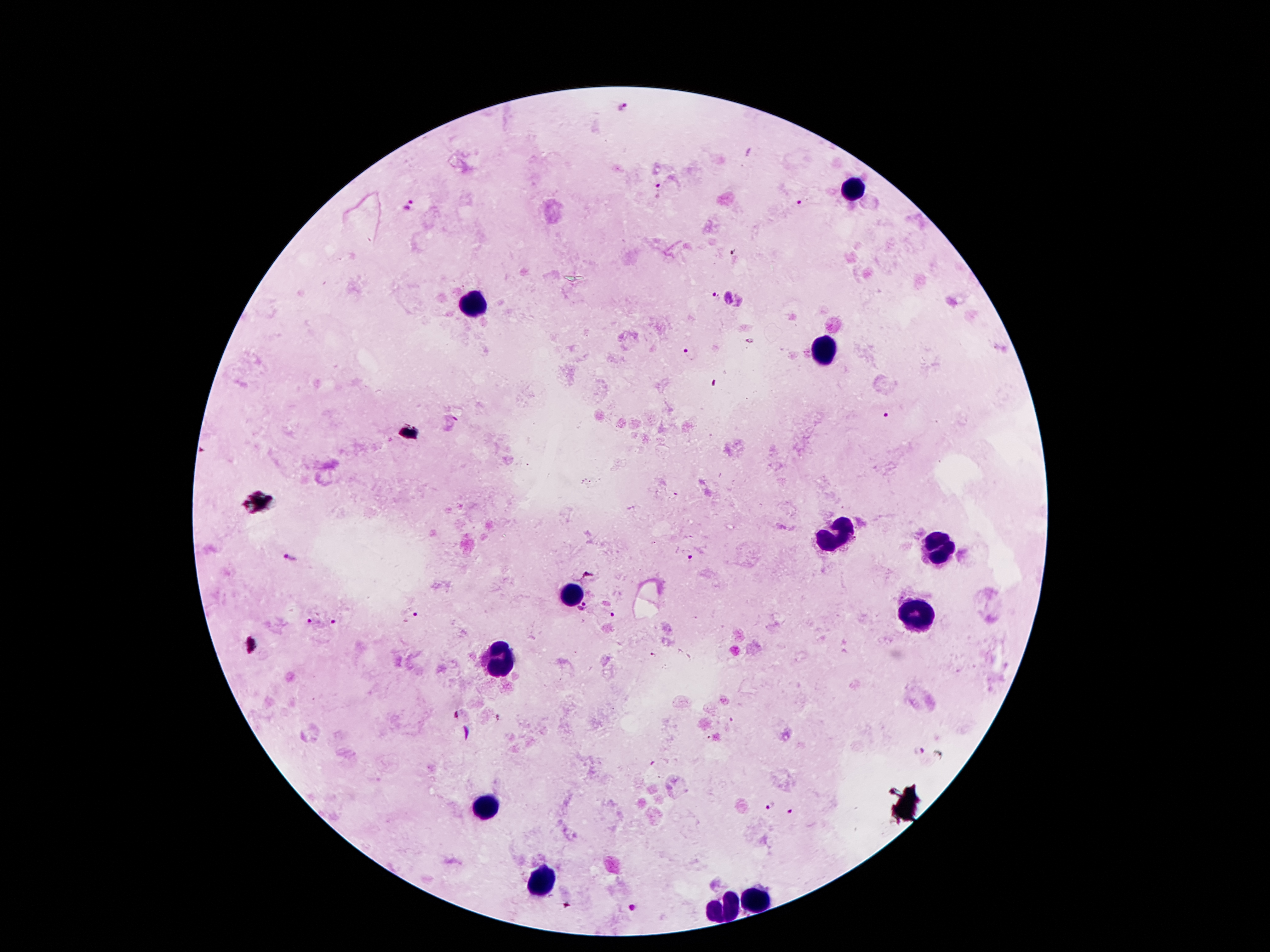

Approximate centers as (x, y) in pixels. Malaria parasite locations: (660, 187), (802, 201), (408, 207), (733, 251), (716, 295), (688, 353), (715, 383), (887, 416), (289, 557), (689, 558), (583, 607), (613, 615), (419, 616), (309, 621), (331, 622), (654, 654), (917, 751), (771, 806), (791, 811), (631, 909). Leukocyte locations: (851, 189), (474, 304), (827, 352), (843, 534), (939, 552), (575, 595), (915, 615), (497, 656), (485, 810), (545, 882), (756, 899), (720, 909). Giemsa-stained preparation. Single field of view. Thick peripheral-blood smear. Photographed through the microscope eyepiece with a smartphone camera. Image is 1270×952 pixels. 100x magnification. Patient malaria status: positive for Plasmodium falciparum.